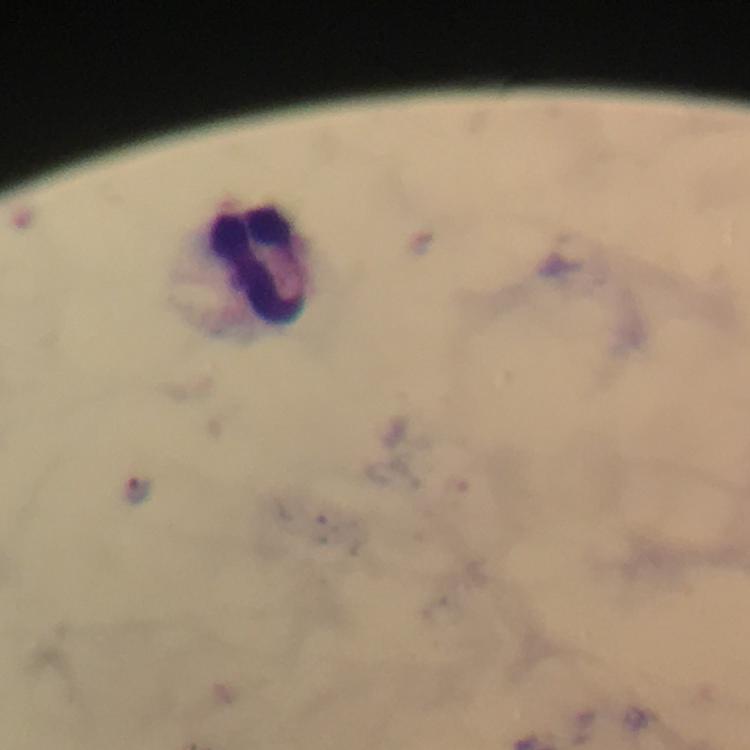

Approximate centers as [x, y] in pixels.
Summary:
  - Plasmodium parasite locations: [139, 490]
  - Leukocyte locations: [266, 267]
  - Preparation: thick blood film
  - Stain: Giemsa
  - Context: from a malaria diagnostic workup
  - Immersion oil: used
  - Cropped from: a single field of view
  - Capture: smartphone mounted on the microscope
  - Image size: 750×750 pixels
  - Magnification: 100x